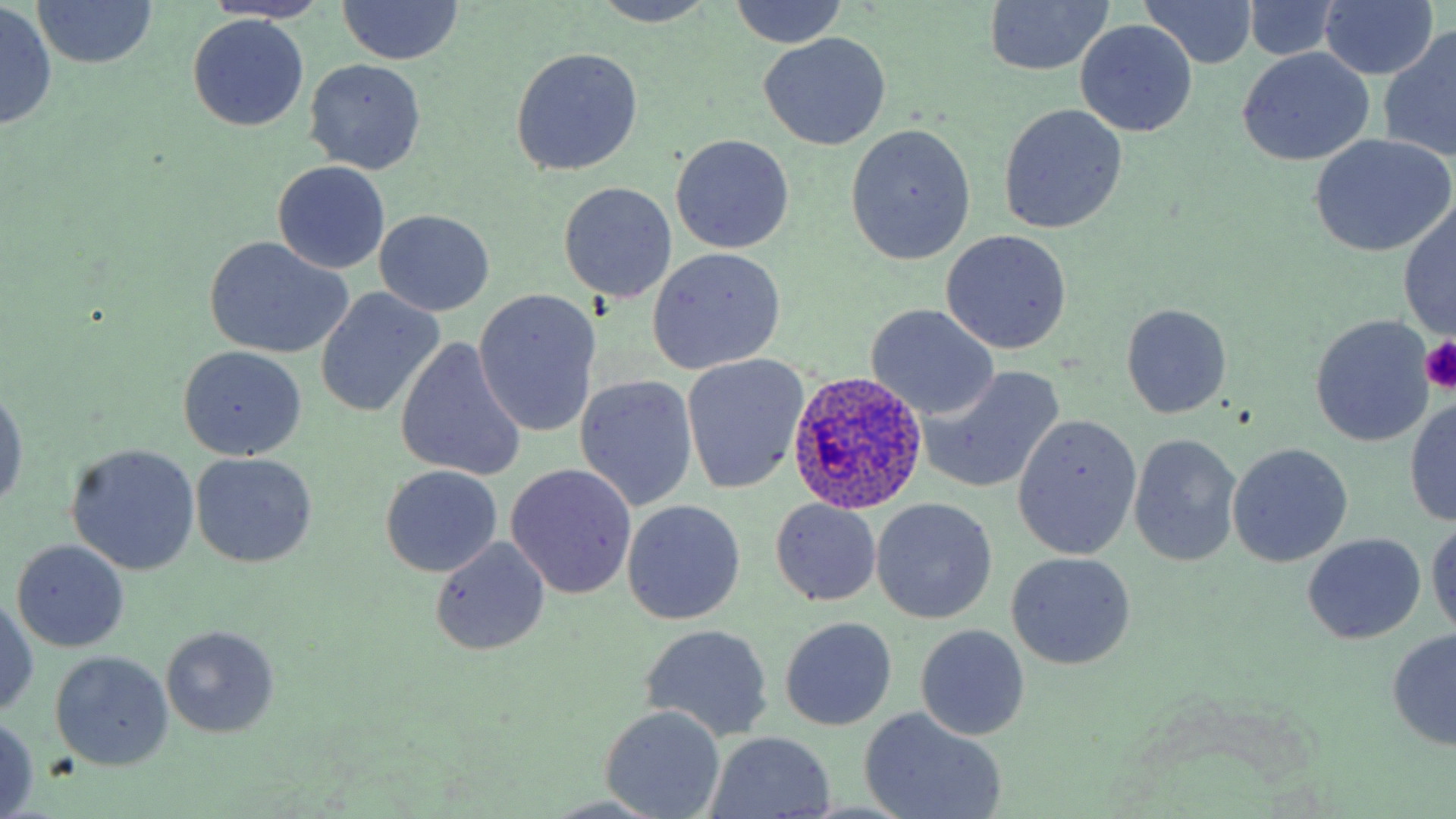

Summary:
  - Coordinate format: approximate bounding boxes as [x1, y1, x2, y2] in pixels
  - Plasmodium ovale-infected red blood cell locations: [785, 372, 931, 513]
  - Platelet locations: [1421, 336, 1455, 394]
  - Uninfected red blood cell locations: [337, 0, 463, 67], [726, 0, 851, 50], [1140, 0, 1258, 70], [593, 1, 718, 27], [982, 1, 1115, 76], [31, 2, 160, 70], [201, 2, 335, 25], [1241, 2, 1343, 60], [1318, 2, 1438, 81], [0, 4, 58, 132], [187, 15, 309, 131], [1075, 21, 1197, 138], [1381, 26, 1456, 164], [760, 33, 891, 151], [510, 47, 643, 177], [1236, 49, 1374, 166], [304, 59, 425, 174], [998, 104, 1128, 235], [847, 127, 975, 263], [1309, 134, 1455, 257], [671, 135, 795, 253], [273, 161, 390, 275], [560, 181, 677, 303], [1398, 203, 1456, 338], [375, 211, 495, 317], [941, 230, 1072, 354], [204, 238, 352, 359], [648, 247, 787, 374], [316, 289, 444, 418], [473, 289, 601, 440], [866, 303, 999, 420], [1120, 303, 1233, 418], [1310, 316, 1434, 447], [396, 337, 526, 482], [178, 345, 307, 461], [681, 355, 809, 493], [918, 367, 1064, 492], [576, 375, 699, 511], [0, 385, 25, 515], [1405, 398, 1456, 525], [1014, 413, 1141, 559], [1129, 433, 1243, 567], [66, 443, 201, 575], [1227, 443, 1353, 566], [191, 453, 316, 569], [506, 464, 636, 598], [381, 467, 502, 577], [872, 498, 997, 623], [622, 499, 746, 624], [770, 500, 882, 606], [1426, 519, 1456, 642], [1302, 533, 1427, 644], [430, 537, 552, 655], [13, 540, 130, 651], [1007, 552, 1135, 670], [1, 591, 40, 720], [780, 617, 897, 729], [642, 623, 773, 740], [916, 624, 1030, 741], [160, 625, 279, 739], [1387, 628, 1456, 749], [49, 650, 174, 770], [601, 706, 725, 818], [861, 710, 1004, 817], [0, 715, 41, 818], [707, 731, 835, 817]
  - Slide-level diagnosis: Plasmodium ovale
  - Magnification: 1000x
  - Modality: light microscopy
  - Image size: 1456×819 pixels
  - Stain: May-Grünwald-Giemsa
  - Preparation: thin blood film
  - Field of view: single